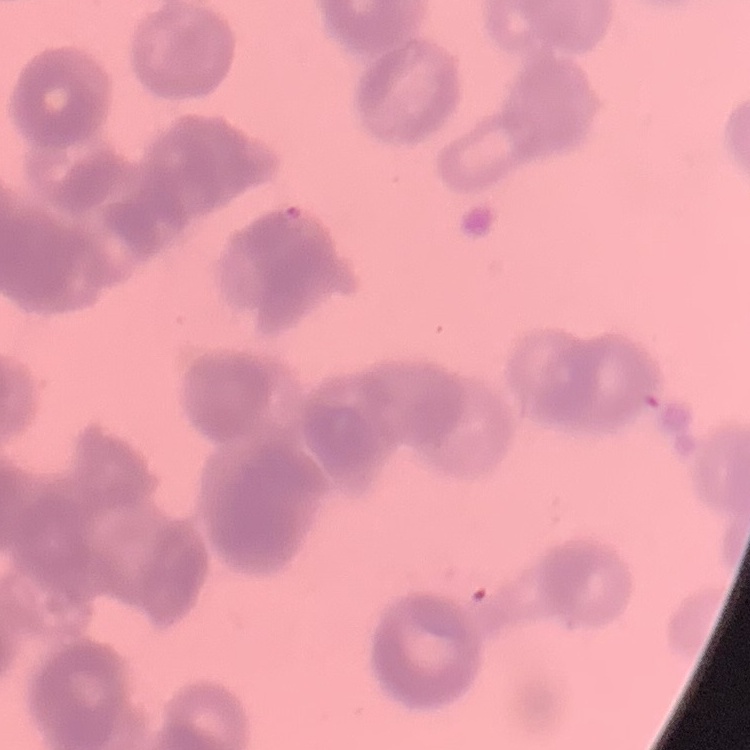
Summary:
  - Red blood cell morphology: rouleaux formation
  - Preparation: thin peripheral smear
  - Stain: Field's or Giemsa
  - Image type: one tile cut from a larger photomicrograph